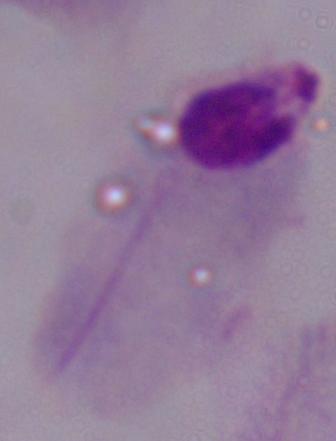

Summary:
  - Modality: photomicrograph
  - Magnification: 1000x
  - Identification: trichomonad